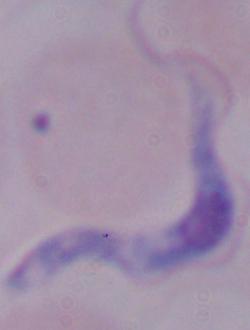

magnification = 1000x
identification = trypanosome
modality = photomicrograph